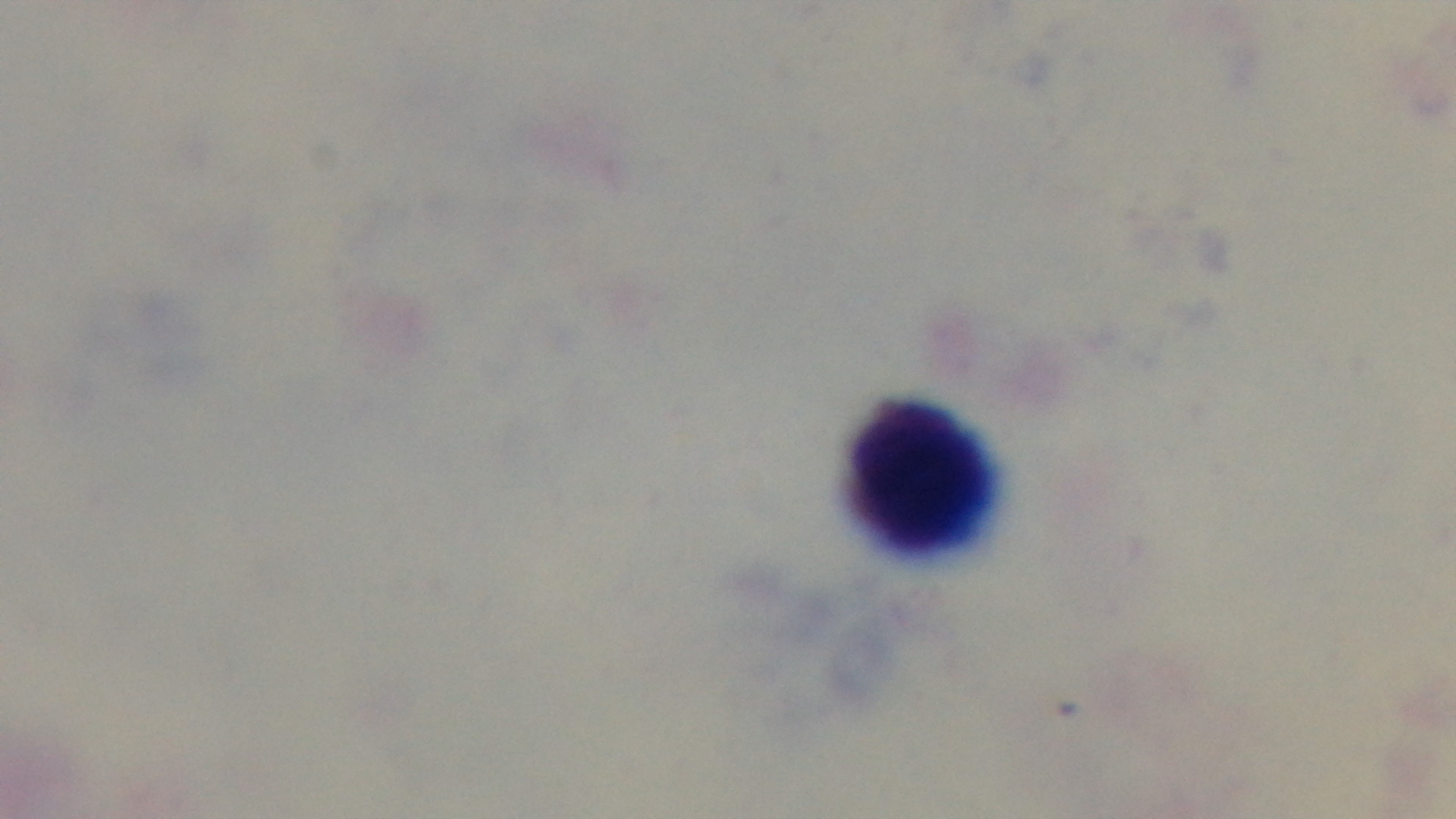

Summary:
  - Preparation: thick
  - Objective: 100x oil immersion
  - Capture: mounted 4K digital camera
  - Modality: light microscopy
  - Malaria status: negative
  - Stain: Giemsa
  - Field of view: one from the slide